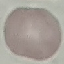
Malaria status: uninfected. Thin smear of blood. Giemsa-stained preparation. Cell patch, automatically extracted from a larger field of view and resized to 64 × 64 pixels. Acquired by smartphone through the microscope eyepiece.